Give the position of every malaria parasite and every leukocyte.
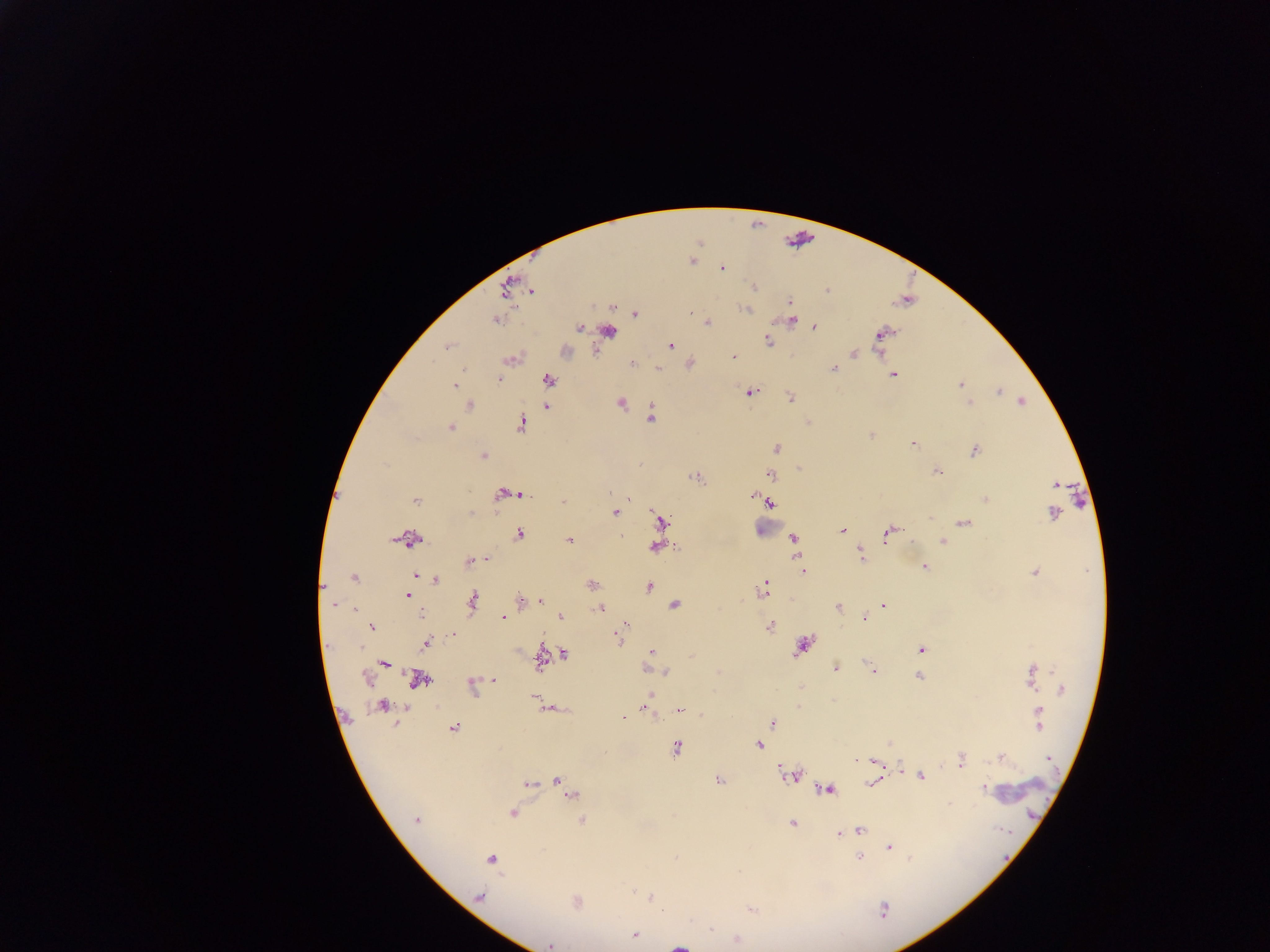

Approximate centers as (x, y) in pixels.
Malaria parasites: (692, 260), (722, 269), (754, 286), (506, 289), (531, 290), (827, 290), (789, 302), (613, 307), (747, 309), (690, 313), (635, 314), (494, 319), (791, 320), (707, 322), (580, 327), (814, 327), (608, 332), (882, 333), (769, 341), (670, 346), (447, 347), (854, 354), (732, 357), (511, 359), (632, 364), (658, 368), (833, 369), (893, 375), (499, 379), (549, 380), (961, 384), (454, 385), (750, 392), (999, 392), (790, 398), (1022, 401), (970, 402), (620, 403), (470, 405), (546, 405), (652, 418), (521, 424), (450, 429), (871, 435), (913, 443), (776, 448), (974, 450), (483, 455), (799, 469), (937, 472), (771, 474), (695, 477), (1055, 484), (610, 492), (502, 494), (510, 494), (522, 495), (751, 495), (985, 499), (415, 500), (629, 500), (563, 501), (770, 503), (1053, 512), (470, 513), (615, 513), (661, 522), (965, 523), (842, 531), (888, 533), (518, 534), (793, 538), (411, 539), (570, 541), (942, 541), (655, 546), (861, 554), (486, 560), (470, 562), (924, 567), (802, 571), (1034, 572), (416, 575), (354, 578), (436, 579), (592, 585), (648, 587), (762, 589), (407, 595), (521, 600), (541, 600), (472, 601), (333, 605), (674, 605), (884, 606), (838, 607), (599, 608), (422, 617), (502, 617), (560, 617), (865, 618), (624, 625), (770, 626), (372, 627), (619, 638), (426, 643), (802, 646), (921, 650), (652, 652), (565, 655), (541, 658), (384, 663), (870, 666), (835, 669), (874, 670), (666, 672), (1031, 675), (918, 677), (366, 678), (495, 679), (418, 680), (472, 686), (1062, 689), (650, 695), (534, 698), (382, 707), (550, 709), (645, 709), (680, 711), (623, 716), (1039, 718), (772, 722), (453, 728), (759, 745), (676, 748), (1002, 757), (1049, 759), (960, 760), (874, 762), (900, 765), (791, 775), (921, 776), (719, 779), (557, 780), (871, 783), (528, 784), (563, 784), (983, 788), (827, 789), (572, 795), (512, 812), (416, 820), (582, 821), (793, 823), (860, 830), (853, 831), (839, 834), (889, 847), (677, 858), (859, 858), (491, 859), (633, 890), (479, 896), (650, 897), (576, 902), (751, 909), (884, 909), (635, 935), (736, 940), (550, 945).
Leukocytes: (772, 525), (1025, 787).
One object is labeled both malaria parasite and leukocyte by the source: (679, 945).

Summary:
  - Country: Ghana
  - Field of view: single
  - Preparation: thick blood film
  - Image size: 1270×952 pixels
  - Capture: mobile-phone photograph through a microscope